Name the parasite shown.
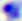
Toxoplasma gondii.

modality = micrograph
magnification = 400x